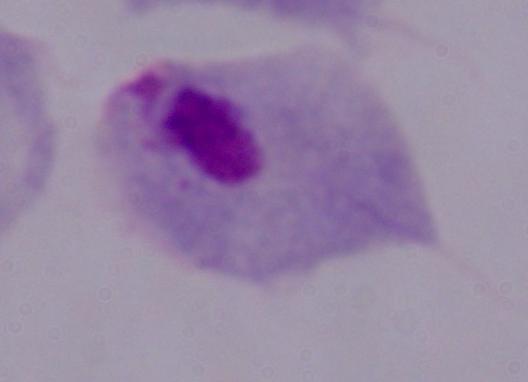 A trichomonad is seen. Micrograph. 1000x magnification.